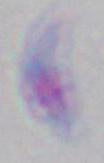
Summary:
  - Magnification: 1000x
  - Modality: micrograph
  - Identification: Toxoplasma gondii